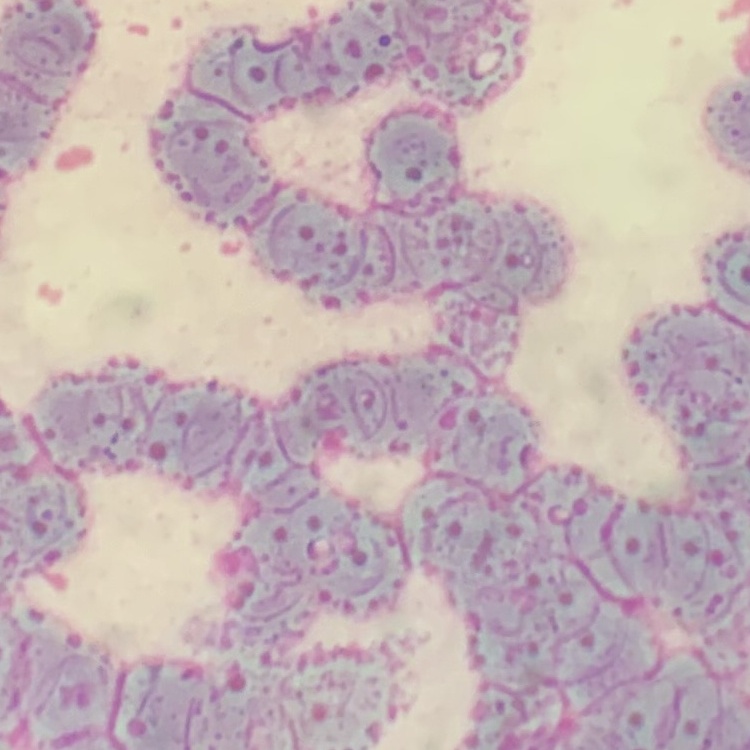
red blood cell morphology = rouleaux formation
image type = one tile cut from a larger photomicrograph
preparation = thin peripheral smear
stain = Field's or Giemsa